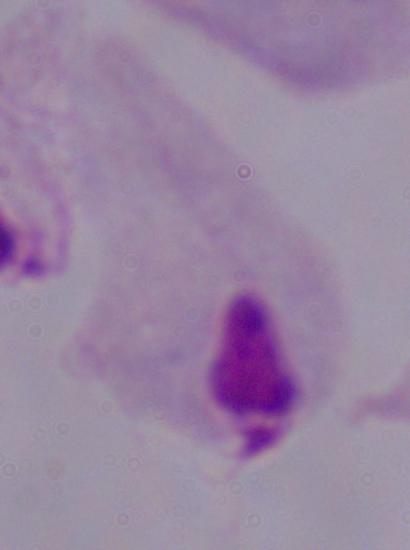
Summary:
  - Magnification: 1000x
  - Modality: photomicrograph
  - Identification: trichomonad